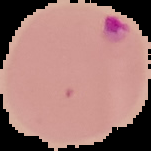
Summary:
  - Image size: 151×151 pixels
  - Preparation: thin blood smear
  - Result: malaria parasites identified
  - Image type: cell region segmented out of the field of view; surrounding area masked to black